Identify the parasite.
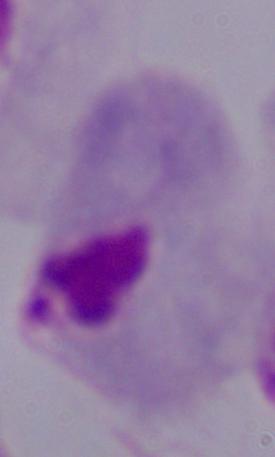

This is a trichomonad.

Photomicrograph. 1000x magnification.